Locate every blood parasite and identify its species.
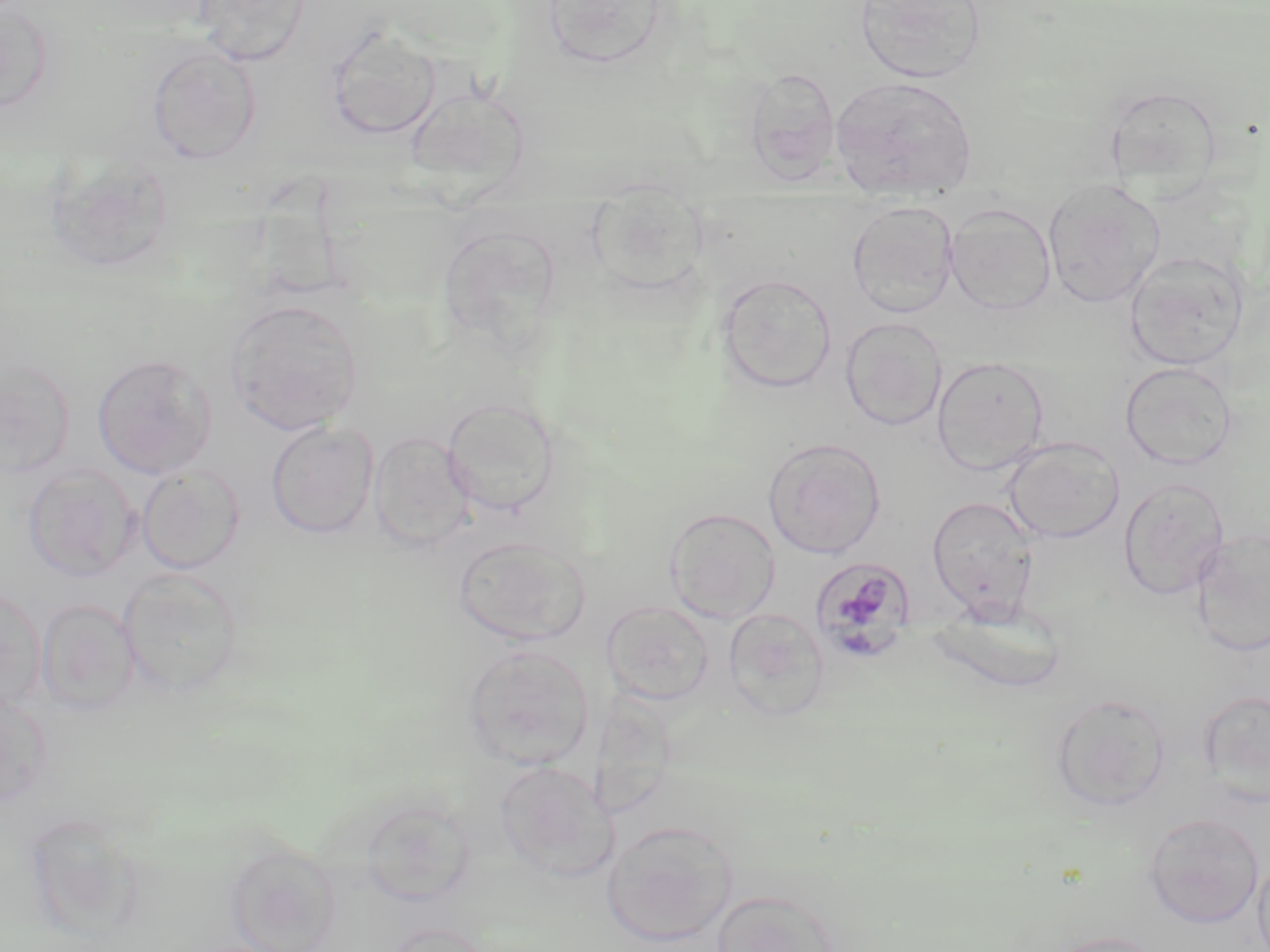

Approximate bounding boxes as (x1, y1, x2, y2) in pixels.
Plasmodium malariae-infected red blood cells: (809, 557, 917, 664).
No Plasmodium falciparum, Plasmodium ovale, Plasmodium vivax, Babesia divergens, or Trypanosoma brucei observed.

{
  "slide_level_diagnosis": "Plasmodium malariae",
  "field_of_view": "single",
  "magnification": "1000x",
  "preparation": "thin blood smear",
  "uninfected_red_blood_cell_locations": "approximate bounding boxes as (x1, y1, x2, y2) in pixels: (193, 0, 310, 67), (541, 0, 672, 70), (854, 0, 988, 85), (0, 3, 52, 113), (325, 27, 441, 140), (147, 46, 262, 164), (743, 67, 841, 184), (828, 75, 979, 201), (406, 82, 532, 196), (1042, 177, 1166, 309), (587, 181, 710, 297), (847, 200, 959, 318), (944, 202, 1056, 316), (1124, 252, 1248, 371), (716, 273, 837, 395), (225, 298, 363, 434), (840, 317, 946, 431), (92, 352, 217, 479), (932, 356, 1050, 475), (0, 357, 76, 480), (1120, 361, 1238, 470), (442, 397, 560, 517), (266, 421, 379, 539), (368, 431, 475, 552), (763, 437, 886, 559), (1003, 437, 1124, 544), (22, 464, 140, 582), (136, 464, 245, 574), (1118, 477, 1230, 601), (926, 496, 1039, 623), (664, 507, 781, 625), (1190, 529, 1270, 658), (452, 535, 590, 647), (118, 568, 244, 697), (0, 586, 46, 710), (36, 599, 140, 717), (601, 599, 715, 706), (929, 604, 1068, 695), (723, 608, 830, 721), (461, 644, 595, 770), (0, 689, 52, 807), (1199, 689, 1270, 804), (1050, 693, 1172, 812), (495, 760, 616, 883), (359, 796, 477, 908), (1143, 812, 1265, 928), (602, 820, 739, 946), (225, 842, 342, 952), (1254, 854, 1270, 952), (709, 888, 842, 952), (383, 922, 493, 952), (1038, 931, 1168, 952)",
  "stain": "May-Grünwald-Giemsa",
  "modality": "optical microscopy",
  "image_size": "1270×952 pixels"
}